Outline each Plasmodium falciparum-infected red blood cell.
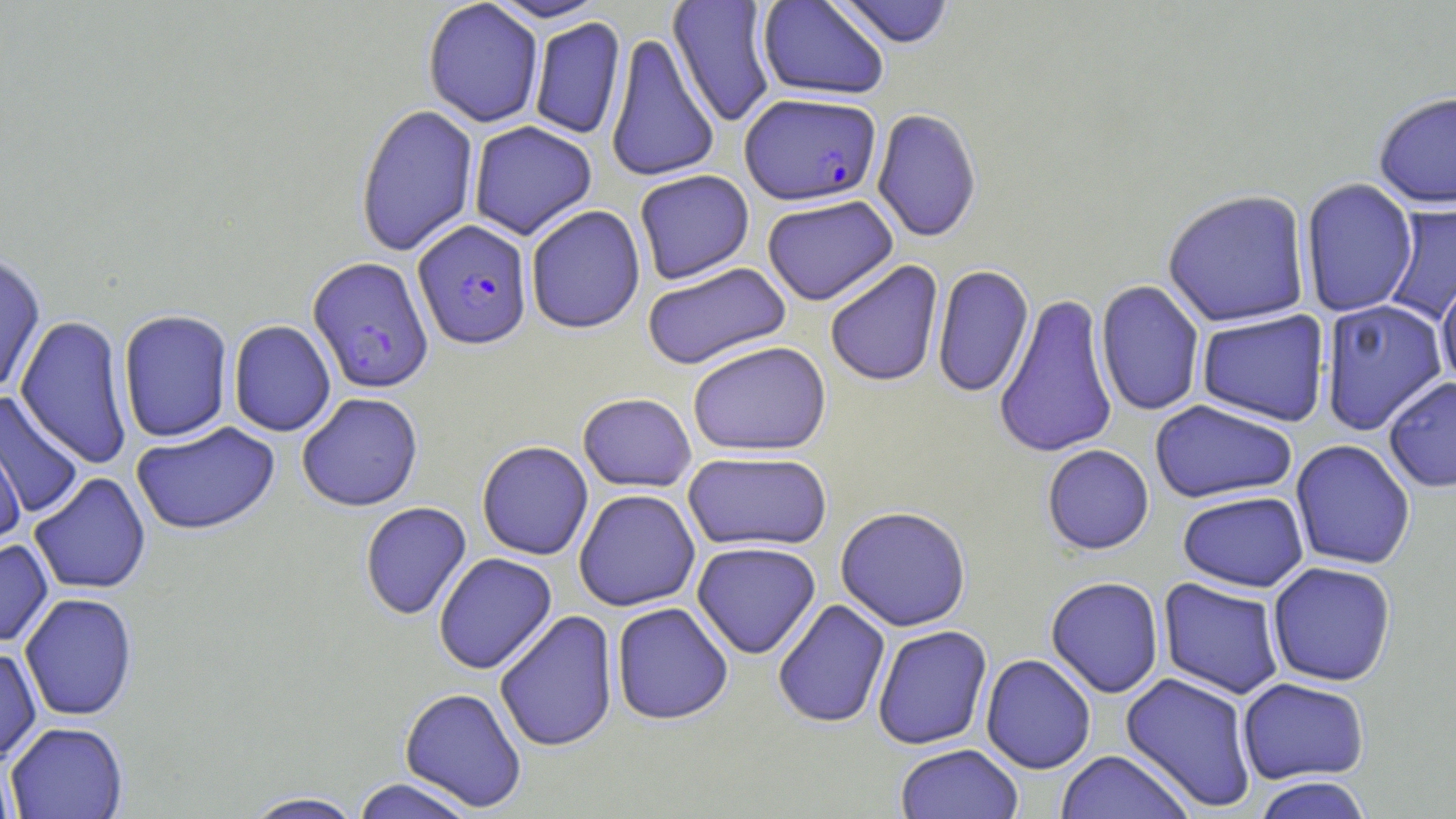

Approximate bounding boxes as named x1/y1/x2/y2 corners in pixels.
Plasmodium falciparum-infected red blood cells: (x1=740, y1=95, x2=881, y2=207), (x1=412, y1=220, x2=533, y2=351), (x1=307, y1=257, x2=434, y2=394).

slide-level diagnosis = Plasmodium falciparum
magnification = 1000x
field of view = single
image size = 1456×819 pixels
preparation = thin blood smear
uninfected red blood cell locations = approximate bounding boxes as named x1/y1/x2/y2 corners in pixels: (x1=484, y1=0, x2=610, y2=23), (x1=667, y1=0, x2=778, y2=127), (x1=757, y1=0, x2=889, y2=101), (x1=830, y1=0, x2=957, y2=49), (x1=423, y1=1, x2=543, y2=128), (x1=528, y1=17, x2=626, y2=140), (x1=605, y1=32, x2=720, y2=183), (x1=1373, y1=91, x2=1456, y2=210), (x1=355, y1=102, x2=479, y2=258), (x1=871, y1=109, x2=982, y2=244), (x1=468, y1=121, x2=597, y2=241), (x1=634, y1=170, x2=755, y2=285), (x1=1300, y1=178, x2=1418, y2=318), (x1=1162, y1=189, x2=1311, y2=328), (x1=762, y1=196, x2=898, y2=306), (x1=1384, y1=200, x2=1456, y2=324), (x1=525, y1=205, x2=646, y2=335), (x1=0, y1=251, x2=46, y2=395), (x1=824, y1=259, x2=944, y2=388), (x1=642, y1=262, x2=792, y2=371), (x1=931, y1=265, x2=1034, y2=398), (x1=1435, y1=276, x2=1456, y2=391), (x1=1095, y1=279, x2=1205, y2=417), (x1=993, y1=293, x2=1119, y2=459), (x1=1319, y1=299, x2=1449, y2=435), (x1=117, y1=310, x2=233, y2=443), (x1=1196, y1=310, x2=1330, y2=427), (x1=15, y1=315, x2=134, y2=468), (x1=228, y1=319, x2=336, y2=437), (x1=687, y1=341, x2=832, y2=456), (x1=1383, y1=376, x2=1456, y2=492), (x1=0, y1=392, x2=84, y2=519), (x1=296, y1=392, x2=423, y2=512), (x1=577, y1=393, x2=697, y2=492), (x1=1149, y1=400, x2=1298, y2=503), (x1=131, y1=421, x2=280, y2=537), (x1=0, y1=433, x2=26, y2=546), (x1=1290, y1=439, x2=1416, y2=570), (x1=476, y1=441, x2=594, y2=560), (x1=1041, y1=444, x2=1154, y2=555), (x1=683, y1=451, x2=832, y2=553), (x1=29, y1=472, x2=151, y2=595), (x1=573, y1=489, x2=700, y2=612), (x1=1177, y1=490, x2=1309, y2=592), (x1=359, y1=502, x2=472, y2=621), (x1=834, y1=506, x2=972, y2=632), (x1=0, y1=537, x2=54, y2=648), (x1=691, y1=541, x2=821, y2=659), (x1=433, y1=553, x2=558, y2=674), (x1=1267, y1=561, x2=1397, y2=687), (x1=1045, y1=576, x2=1164, y2=698), (x1=1157, y1=578, x2=1286, y2=700), (x1=20, y1=592, x2=138, y2=722), (x1=772, y1=599, x2=891, y2=728), (x1=611, y1=602, x2=734, y2=725), (x1=495, y1=610, x2=618, y2=753), (x1=872, y1=625, x2=993, y2=750), (x1=0, y1=647, x2=42, y2=766), (x1=980, y1=654, x2=1096, y2=774), (x1=1120, y1=671, x2=1258, y2=812), (x1=1237, y1=677, x2=1370, y2=785), (x1=399, y1=686, x2=527, y2=812), (x1=5, y1=721, x2=128, y2=819), (x1=895, y1=744, x2=1024, y2=819), (x1=1055, y1=750, x2=1196, y2=819), (x1=0, y1=759, x2=18, y2=819), (x1=1252, y1=776, x2=1373, y2=819), (x1=350, y1=778, x2=479, y2=819), (x1=240, y1=791, x2=368, y2=818)
modality = light microscopy
stain = May-Grünwald-Giemsa